Report the malaria status of this cell.
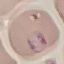
It is parasitized.

image type = cell patch, automatically extracted from a larger field of view and resized to 64 × 64 pixels
capture = smartphone through the microscope eyepiece
stain = Giemsa
preparation = thin blood film